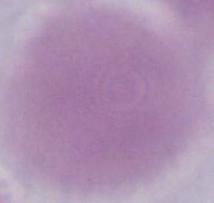 An erythrocyte is seen. 1000x magnification. Photomicrograph.